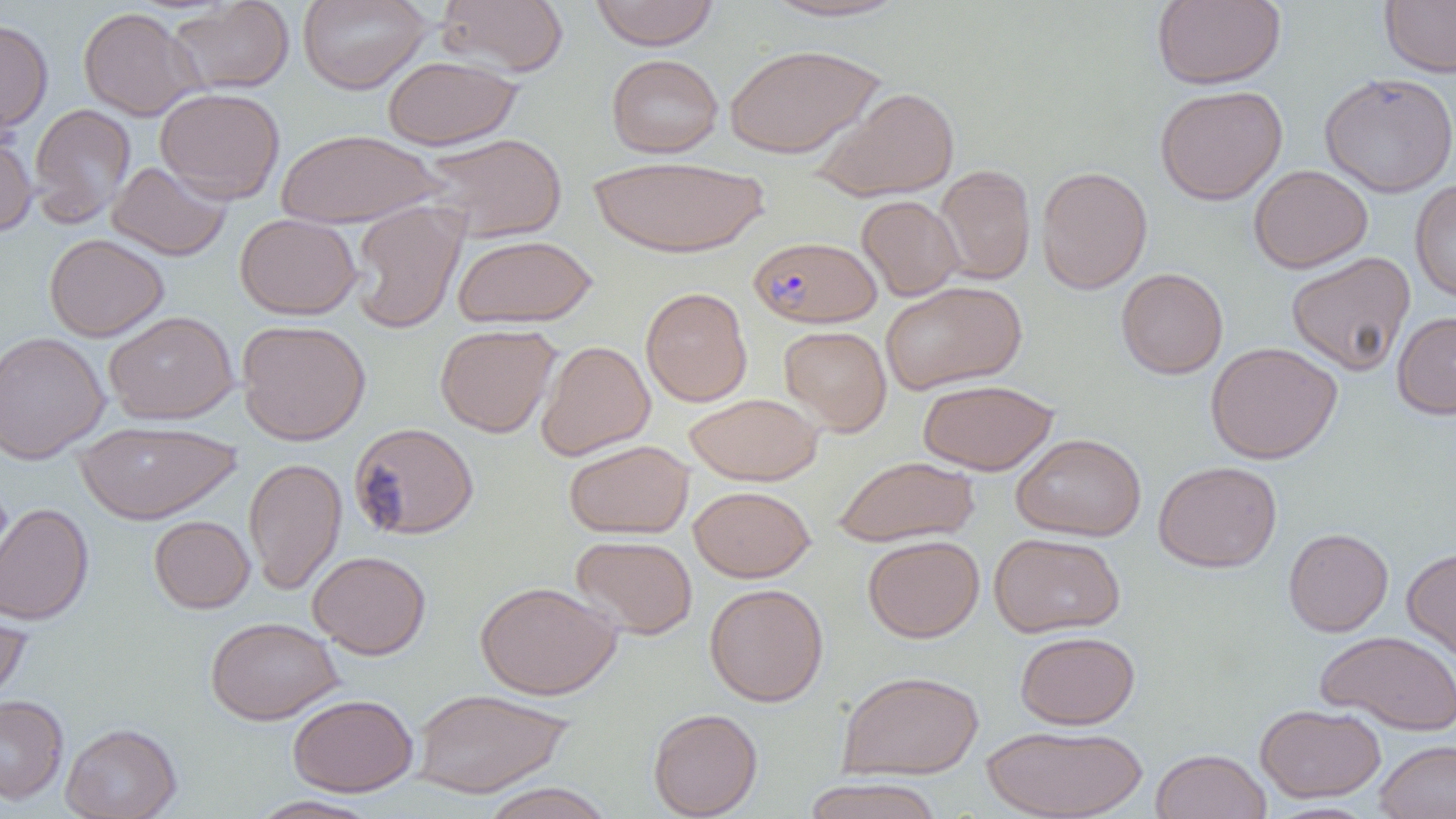
Approximate bounding boxes as (x1,y1)-(x2,y2) corner pairs in pixels. Uninfected red blood cell locations: (166,0)-(295,95), (298,0)-(431,94), (436,0)-(569,77), (590,0)-(719,50), (758,0)-(913,23), (1152,0)-(1286,89), (1379,0)-(1456,77), (78,7)-(203,121), (0,16)-(53,134), (723,44)-(884,159), (600,53)-(737,259), (606,53)-(723,158), (382,54)-(523,150), (1319,72)-(1456,198), (810,85)-(960,202), (1155,85)-(1288,205), (155,87)-(285,203), (29,104)-(136,226), (0,128)-(37,237), (274,128)-(443,228), (420,132)-(567,242), (589,154)-(770,259), (107,161)-(232,261), (934,164)-(1036,284), (1249,164)-(1373,273), (1036,166)-(1152,294), (1410,179)-(1456,302), (856,195)-(964,301), (349,200)-(467,334), (234,213)-(362,320), (44,233)-(169,341), (452,234)-(598,328), (1286,251)-(1416,376), (1116,267)-(1229,379), (880,280)-(1027,394), (640,286)-(753,407), (104,310)-(239,424), (1392,311)-(1456,419), (236,319)-(371,446), (434,324)-(561,437), (778,325)-(892,436), (0,330)-(110,464), (536,340)-(655,460), (1204,341)-(1343,464), (918,379)-(1058,475), (684,392)-(823,485), (74,420)-(242,524), (349,422)-(479,540), (1011,432)-(1146,541), (563,439)-(694,539), (833,455)-(980,547), (244,457)-(347,594), (1153,460)-(1282,573), (688,485)-(815,582), (0,502)-(94,625), (149,515)-(254,613), (1283,528)-(1393,636), (989,532)-(1125,637), (571,534)-(698,640), (862,535)-(985,642), (1401,546)-(1456,663), (307,550)-(431,659), (475,580)-(622,700), (704,583)-(829,707), (0,604)-(32,708), (205,616)-(343,724), (1316,629)-(1456,735), (1015,630)-(1140,729), (837,669)-(984,779), (411,687)-(573,798), (288,693)-(418,796), (0,695)-(69,803), (1255,703)-(1386,802), (648,708)-(762,818), (61,722)-(181,819), (981,724)-(1147,819), (1375,739)-(1456,819), (1150,748)-(1271,819), (801,777)-(945,819), (479,782)-(616,819), (248,795)-(382,819). Plasmodium falciparum-infected red blood cell locations: (749,235)-(882,328). Slide-level diagnosis: Plasmodium falciparum. Thin blood smear. Image is 1456×819 pixels. Light microscopy. Single field of view. Captured at 1000x magnification.